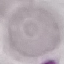

malaria status = uninfected
preparation = thin smear
capture = smartphone camera at the microscope eyepiece
stain = Giemsa
image type = cell patch, automatically extracted from a larger field of view and resized to 64 × 64 pixels